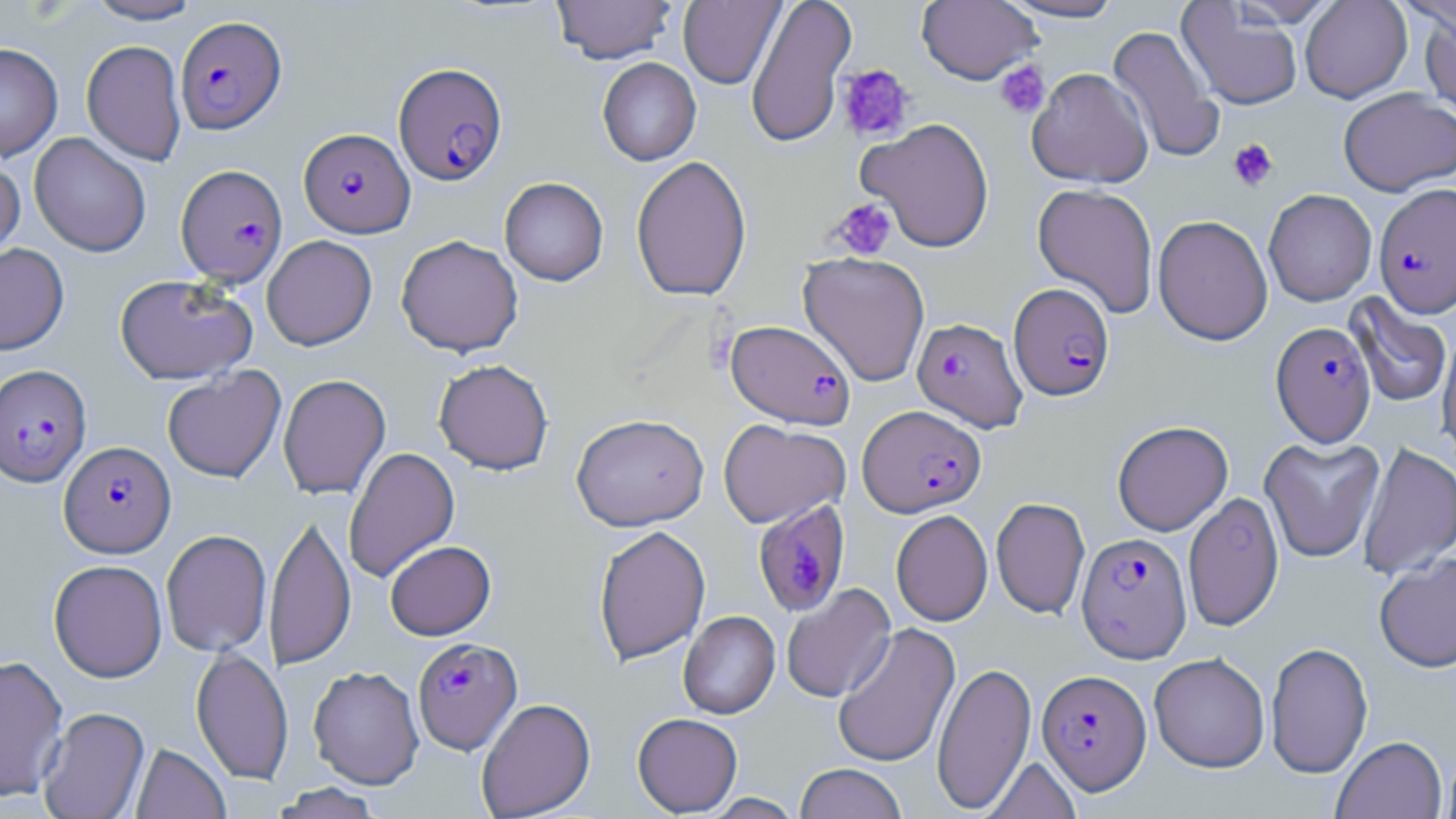
Approximate bounding boxes as (x1,y1)-(x2,y2) corner pairs in pixels. Platelet locations: (994,60)-(1050,119), (837,64)-(915,142), (1227,138)-(1278,191), (828,198)-(897,262). Uninfected red blood cell locations: (84,0)-(203,24), (552,0)-(676,64), (678,0)-(785,89), (745,0)-(857,149), (998,0)-(1128,23), (1227,0)-(1343,26), (1300,0)-(1412,103), (917,1)-(1041,85), (1177,2)-(1303,111), (1420,9)-(1456,124), (1107,25)-(1224,164), (81,40)-(187,165), (0,43)-(63,161), (597,58)-(701,166), (1026,67)-(1153,188), (1338,87)-(1456,196), (857,117)-(995,252), (29,132)-(151,257), (631,155)-(752,302), (0,158)-(25,265), (499,177)-(608,286), (1032,183)-(1159,318), (1263,189)-(1377,306), (1153,214)-(1273,345), (262,235)-(377,350), (396,235)-(524,357), (0,243)-(69,355), (798,251)-(930,387), (115,274)-(257,385), (1345,293)-(1453,409), (1438,329)-(1456,461), (433,358)-(554,475), (162,366)-(286,482), (277,374)-(391,500), (571,412)-(709,531), (718,419)-(850,528), (1112,420)-(1233,536), (1259,435)-(1384,563), (1357,442)-(1456,579), (343,447)-(460,582), (1183,492)-(1284,631), (991,497)-(1090,619), (891,509)-(992,626), (265,510)-(356,672), (592,524)-(711,665), (161,529)-(272,657), (385,540)-(496,640), (1374,553)-(1456,673), (48,559)-(167,682), (781,584)-(896,703), (678,611)-(780,719), (832,622)-(961,769), (1266,641)-(1374,778), (191,646)-(293,785), (1149,652)-(1270,773), (0,654)-(68,802), (932,661)-(1036,814), (308,665)-(424,789), (476,697)-(596,818), (38,706)-(150,819), (632,712)-(743,816), (1331,735)-(1447,819), (130,743)-(231,819), (1440,745)-(1456,819), (981,757)-(1082,818), (795,763)-(907,819), (270,783)-(385,818), (703,793)-(803,818). Plasmodium falciparum-infected red blood cell locations: (175,15)-(286,134), (393,62)-(507,185), (299,128)-(415,237), (176,164)-(287,285), (1374,183)-(1456,318), (1009,282)-(1115,401), (912,317)-(1027,432), (727,319)-(856,429), (1271,321)-(1376,446), (0,364)-(92,487), (858,404)-(986,517), (59,440)-(175,558), (753,499)-(851,617), (1076,531)-(1192,662), (412,637)-(521,754), (1037,669)-(1151,795). Slide-level diagnosis: Plasmodium falciparum. Image is 1456×819 pixels. Optical microscopy. Thin blood smear. 1000x magnification. May-Grünwald-Giemsa-stained preparation. One field of a larger specimen.